State which cell type is depicted.
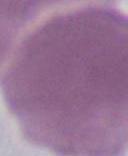
An erythrocyte.

Photomicrograph. 1000x magnification.